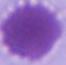
Summary:
  - Identification: erythrocyte
  - Magnification: 1000x
  - Modality: micrograph